Identify the parasite.
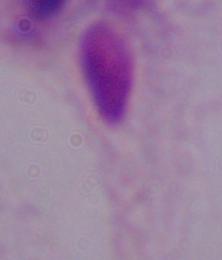

A trichomonad.

modality = micrograph
magnification = 1000x